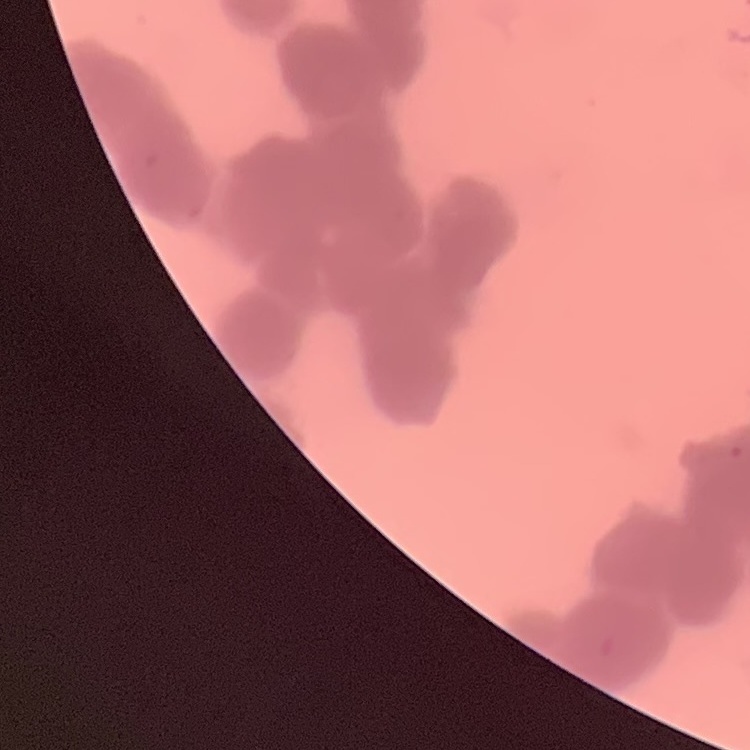

erythrocyte_morphology: rouleaux formation
preparation: thin blood smear
image_type: square crop of a larger photomicrograph
stain: Field's or Giemsa